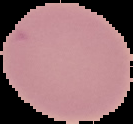
Image is 133×124 pixels. Result: no Plasmodium parasites seen. Segmented cell region on a black background. From a thin blood smear.